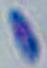

Summary:
  - Identification: Toxoplasma gondii
  - Magnification: 1000x
  - Modality: photomicrograph